Report the malaria status of this cell.
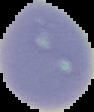
It is uninfected.

image type = segmented cell region on a black background
image size = 94×112 pixels
preparation = thin blood film